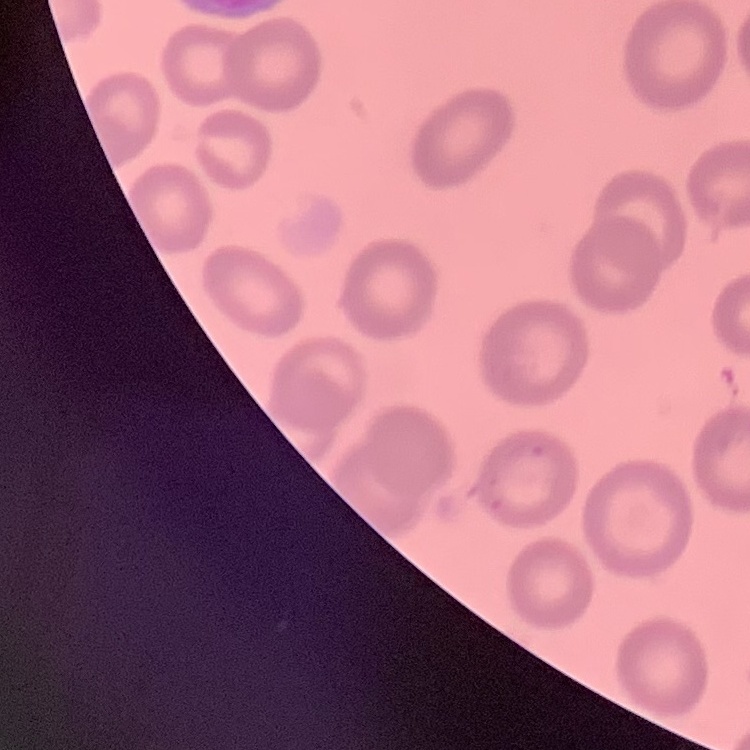
The red blood cells show no rouleaux formation. Field's or Giemsa stain. Thin peripheral smear. One tile cut from a larger photomicrograph.